Point out each leukocyte.
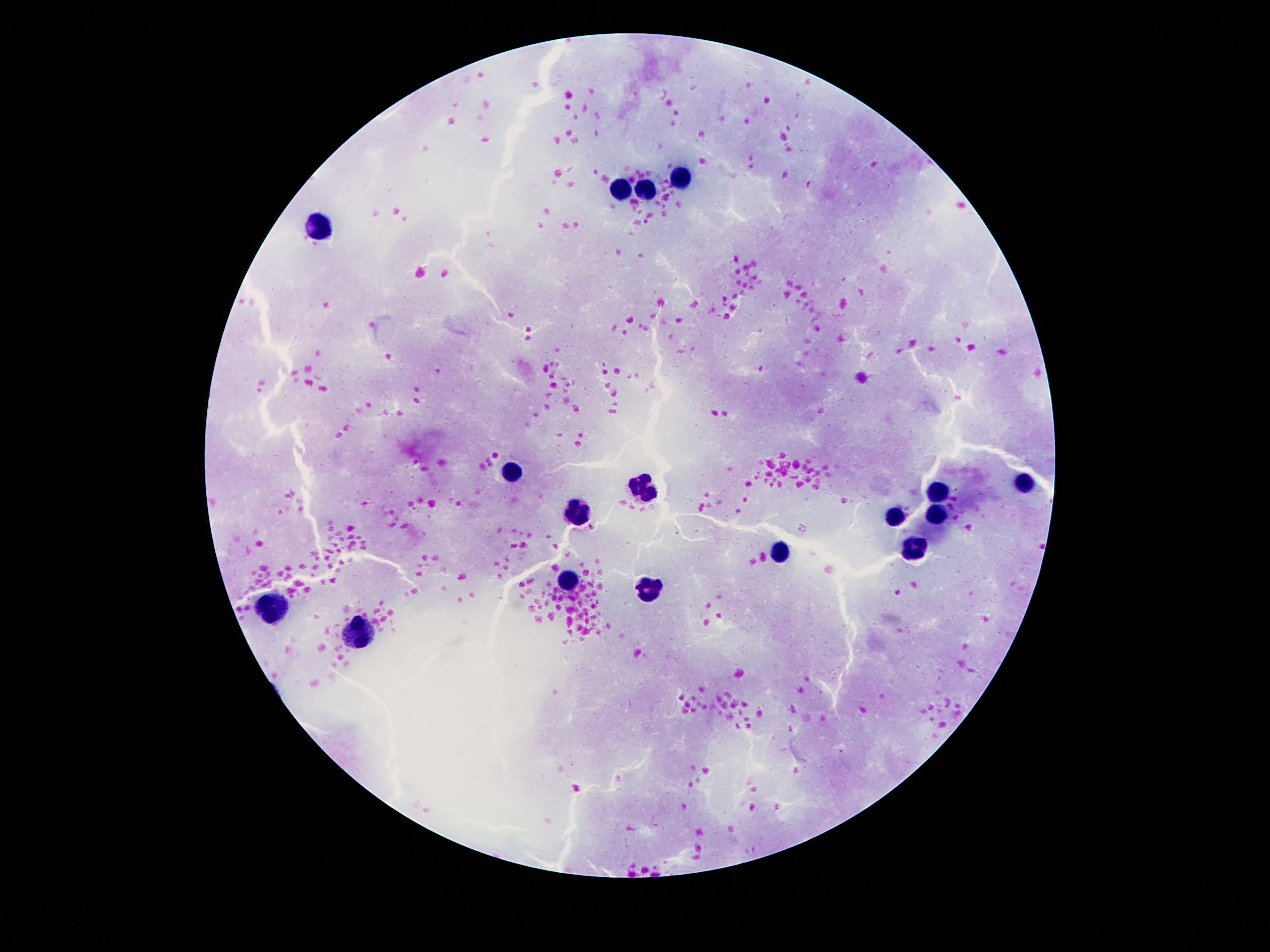
Approximate centers as {x, y} in pixels.
Leukocytes: {678, 178}, {622, 190}, {645, 193}, {319, 231}, {510, 472}, {1024, 483}, {641, 488}, {936, 491}, {938, 512}, {575, 515}, {895, 517}, {911, 547}, {780, 551}, {567, 581}, {645, 590}, {272, 612}, {358, 636}.

{
  "field_of_view": "single",
  "image_size": "1270×952 pixels",
  "magnification": "100x",
  "stain": "Giemsa",
  "patient_malaria_status": "uninfected",
  "preparation": "thick blood film",
  "capture": "smartphone camera through the microscope eyepiece"
}